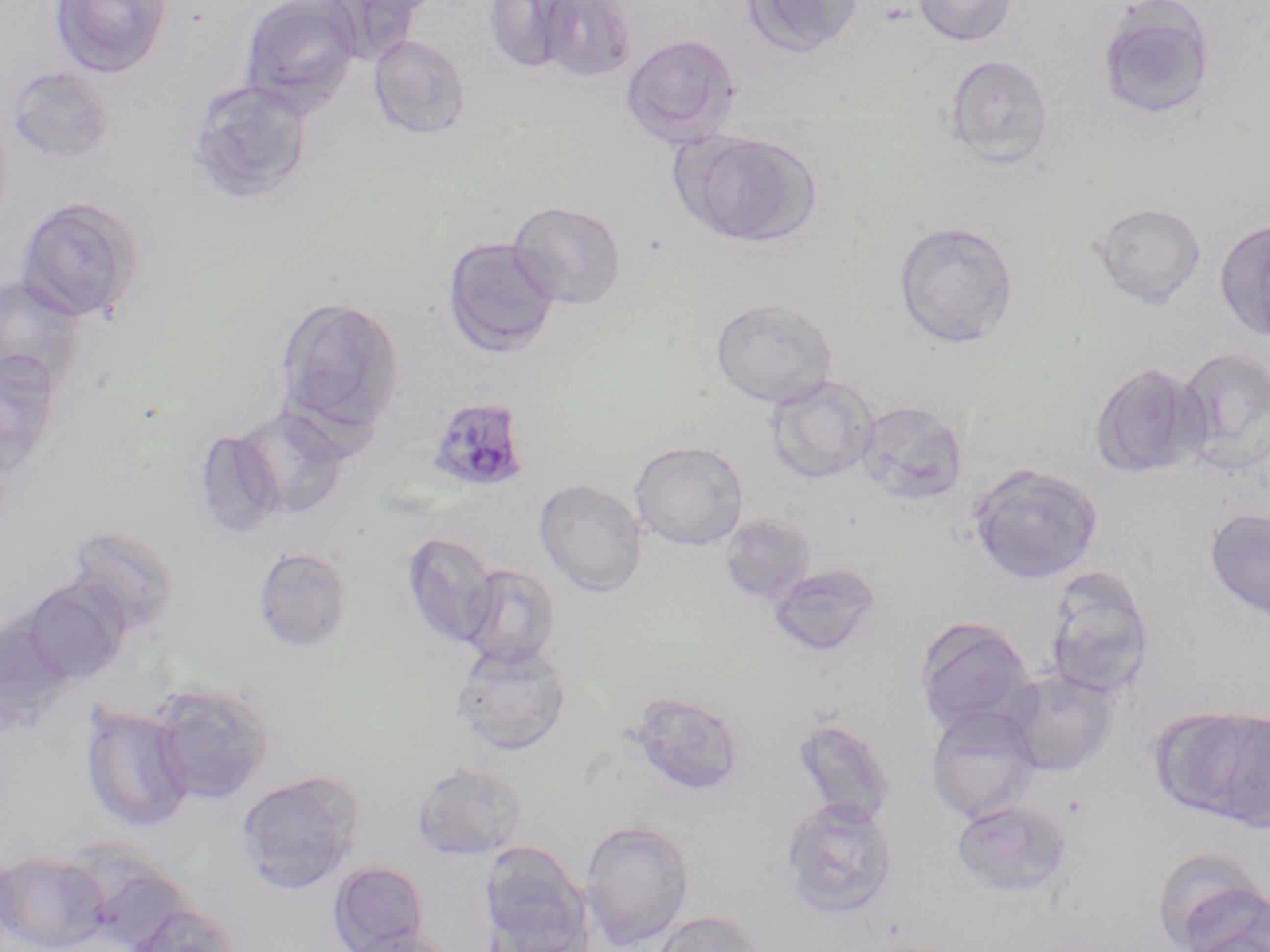

slide-level diagnosis = Plasmodium malariae
magnification = 1000x
Plasmodium malariae-infected red blood cell locations = approximate bounding boxes as [x1, y1, x2, y2] in pixels: [427, 397, 530, 494]
stain = May-Grünwald-Giemsa
preparation = thin blood film
image size = 1270×952 pixels
modality = light microscopy
field of view = single
uninfected red blood cell locations = approximate bounding boxes as [x1, y1, x2, y2] in pixels: [49, 0, 172, 78], [239, 0, 362, 117], [486, 0, 575, 71], [741, 0, 866, 58], [912, 0, 1017, 46], [540, 1, 636, 83], [1095, 1, 1217, 123], [368, 34, 471, 140], [621, 34, 741, 148], [944, 53, 1054, 170], [6, 66, 114, 164], [186, 78, 312, 204], [683, 131, 820, 247], [16, 196, 145, 323], [508, 200, 627, 310], [1093, 202, 1206, 307], [1214, 219, 1270, 342], [893, 220, 1018, 348], [442, 237, 560, 357], [0, 275, 89, 394], [275, 294, 406, 438], [709, 298, 838, 407], [1176, 347, 1270, 475], [0, 350, 63, 478], [1089, 361, 1206, 479], [765, 375, 878, 485], [855, 400, 968, 505], [234, 407, 349, 520], [194, 429, 284, 538], [629, 440, 749, 550], [967, 463, 1104, 584], [533, 478, 648, 596], [1204, 508, 1270, 622], [721, 514, 816, 605], [63, 524, 180, 637], [401, 531, 499, 649], [253, 547, 353, 654], [460, 563, 561, 671], [768, 563, 882, 658], [1045, 569, 1155, 697], [19, 581, 127, 686], [0, 614, 75, 736], [915, 616, 1037, 736], [451, 641, 571, 756], [1004, 667, 1121, 777], [150, 682, 274, 805], [626, 689, 746, 797], [81, 702, 193, 832], [924, 704, 1042, 824], [1155, 705, 1270, 829], [792, 717, 896, 825], [412, 760, 527, 860], [236, 770, 365, 894], [780, 795, 898, 917], [952, 800, 1072, 898], [580, 819, 695, 949], [479, 843, 594, 952], [1152, 849, 1269, 951], [0, 852, 107, 952], [69, 852, 195, 951], [329, 860, 429, 951], [1182, 896, 1270, 952], [125, 901, 243, 952], [649, 910, 764, 952], [345, 928, 460, 952]